Name the blood parasite species.
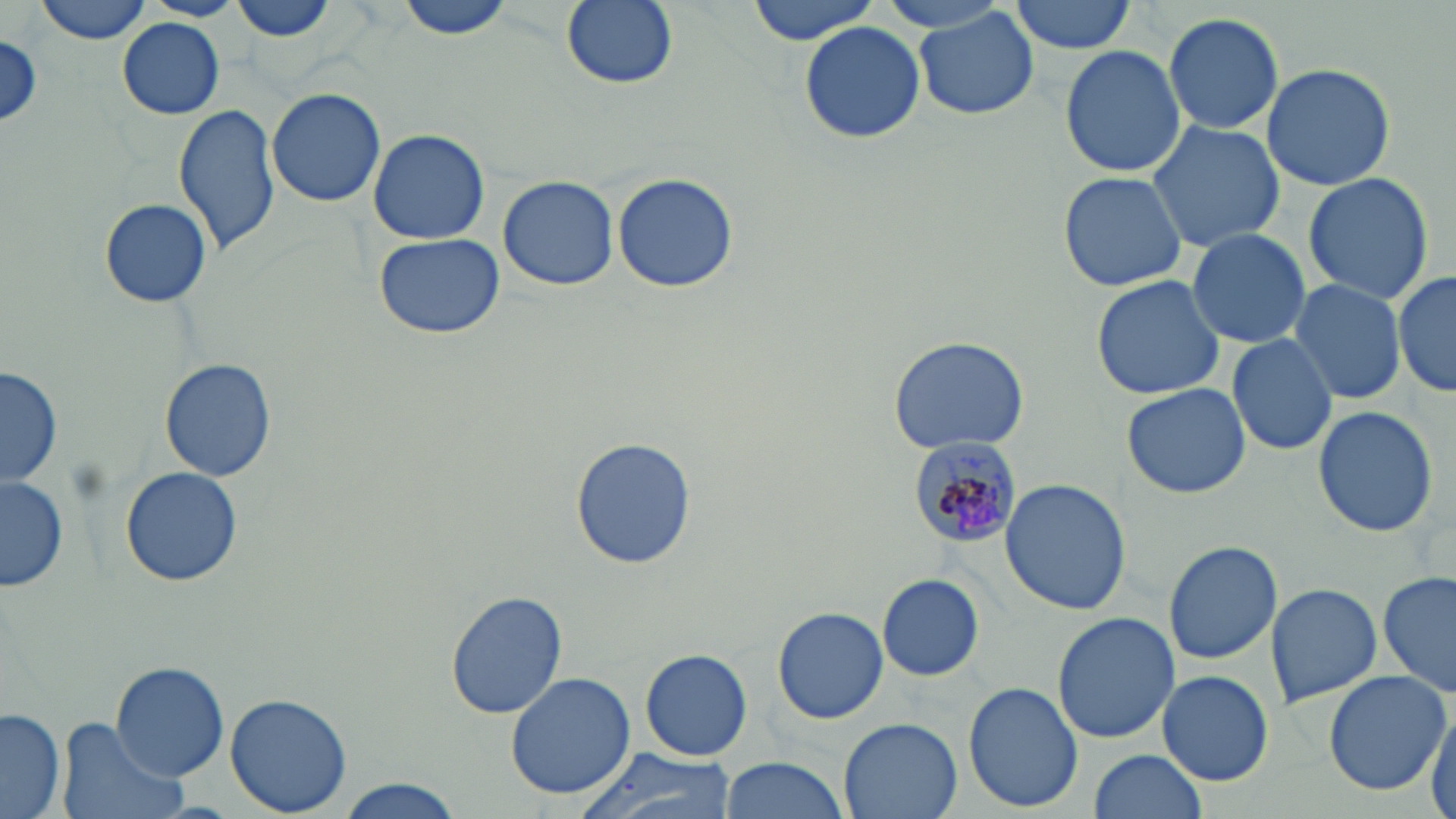

Plasmodium malariae.

modality: light microscopy
preparation: thin blood film
stain: May-Grünwald-Giemsa
uninfected_red_blood_cell_locations: 'approximate bounding boxes as (x1,y1)-(x2,y2) corner pairs in pixels: (34,0)-(155,43), (145,0)-(244,21), (226,0)-(343,47), (395,0)-(515,42), (559,0)-(680,91), (747,0)-(882,45), (1009,0)-(1137,53), (914,8)-(1043,120), (1163,10)-(1286,135), (117,18)-(225,118), (801,22)-(925,143), (1,36)-(43,129), (1059,45)-(1185,177), (1261,62)-(1396,191), (265,87)-(388,208), (173,102)-(283,258), (1146,120)-(1285,251), (368,128)-(490,244), (1058,170)-(1188,293), (1302,171)-(1434,305), (612,172)-(739,294), (497,175)-(620,291), (99,198)-(212,307), (1186,228)-(1312,351), (374,233)-(505,341), (1394,270)-(1456,399), (1090,275)-(1226,402), (1288,278)-(1409,405), (1225,334)-(1339,457), (886,336)-(1032,456), (159,358)-(278,481), (2,364)-(61,489), (1122,384)-(1251,498), (1312,406)-(1440,538), (566,438)-(695,570), (119,465)-(245,587), (1,474)-(68,593), (998,478)-(1130,615), (1163,539)-(1284,664), (1377,571)-(1455,701), (878,575)-(984,682), (1264,582)-(1383,706), (444,590)-(567,719), (773,605)-(888,724), (1052,611)-(1180,743), (640,648)-(753,762), (110,662)-(230,783), (1322,670)-(1451,793), (1156,671)-(1275,786), (505,672)-(636,799), (963,681)-(1083,812), (225,692)-(353,816), (1429,705)-(1456,819), (0,707)-(66,817), (55,717)-(189,819), (839,717)-(962,819), (572,747)-(734,819), (1088,749)-(1208,818), (720,756)-(850,819), (332,777)-(465,819)'
field_of_view: single
image_size: 1456×819 pixels
plasmodium_malariae_infected_red_blood_cell_locations: 'approximate bounding boxes as (x1,y1)-(x2,y2) corner pairs in pixels: (908,435)-(1025,549)'
magnification: 1000x